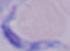

Micrograph. Captured at 1000x magnification. A trypanosome is seen.